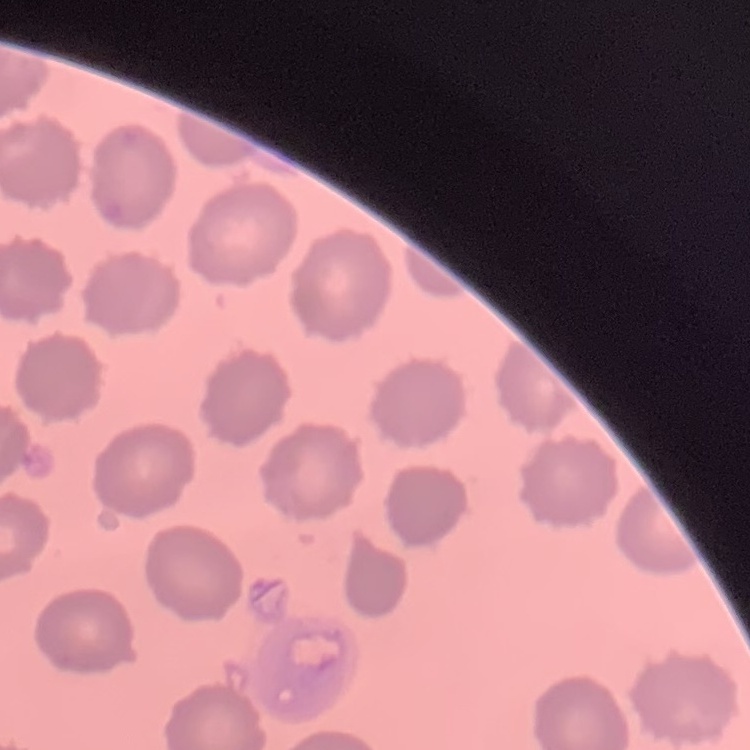
Summary:
  - Erythrocyte morphology: no rouleaux formation
  - Image type: one tile cut from a larger photomicrograph
  - Preparation: thin blood smear
  - Stain: Field's or Giemsa